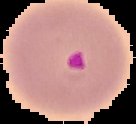
preparation = thin blood film
image type = segmented cell region with the area outside set to black
result = Plasmodium parasites identified
image size = 136×124 pixels